Give the position of every malaria parasite.
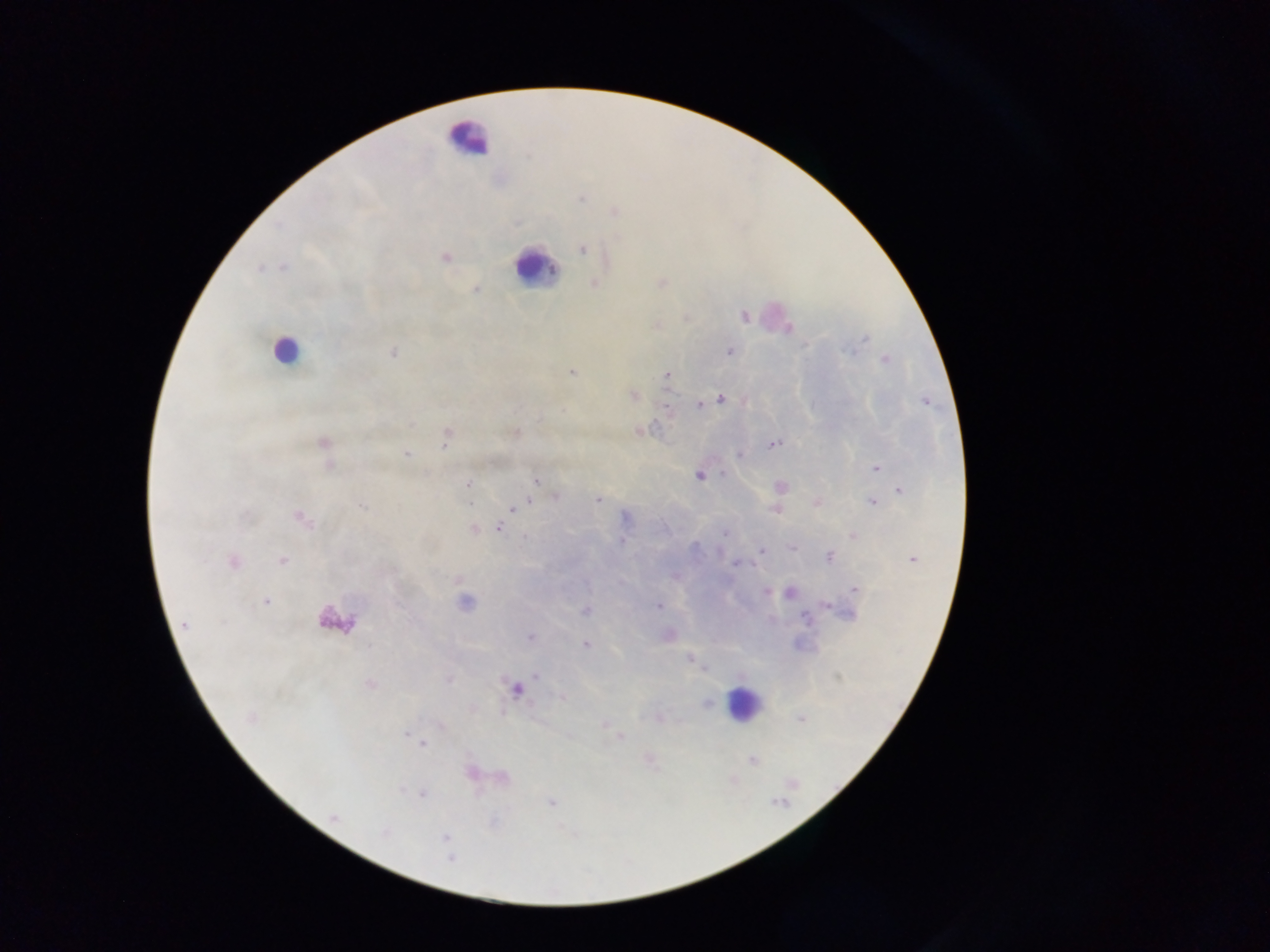
Approximate centers as x y in pixels.
Malaria parasites: 582 198; 583 249; 446 257; 476 289; 743 317; 788 328; 866 339; 729 351; 849 351; 393 352; 885 360; 572 372; 667 375; 633 395; 720 399; 712 401; 926 402; 665 405; 699 405; 640 430; 515 433; 445 439; 324 443; 773 444; 406 453; 739 455; 876 468; 722 474; 699 476; 536 480; 468 484; 779 487; 900 491; 556 496; 598 500; 529 501; 872 502; 815 503; 361 507; 513 509; 774 510; 625 517; 301 519; 473 528; 498 528; 725 533; 852 535; 621 541; 792 547; 761 549; 830 557; 913 559; 282 560; 233 562; 735 563; 855 589; 765 592; 790 593; 266 602; 465 602; 828 605; 658 606; 585 611; 850 615; 806 618; 184 624; 530 637; 585 644; 689 659; 536 675; 449 680; 369 684; 515 690; 562 697; 707 703; 250 718; 801 719; 604 724; 440 726; 407 734; 620 737; 417 740; 423 743; 752 761; 503 777; 793 783; 400 791; 422 794; 551 802; 333 817; 383 833; 445 837; 450 858.

Summary:
  - Leukocyte locations: 465 138; 535 268; 772 317; 284 350; 337 621; 743 703
  - Capture: mobile-phone photograph through a microscope
  - Preparation: thick blood smear
  - Country: Ghana
  - Field of view: single
  - Image size: 1270×952 pixels